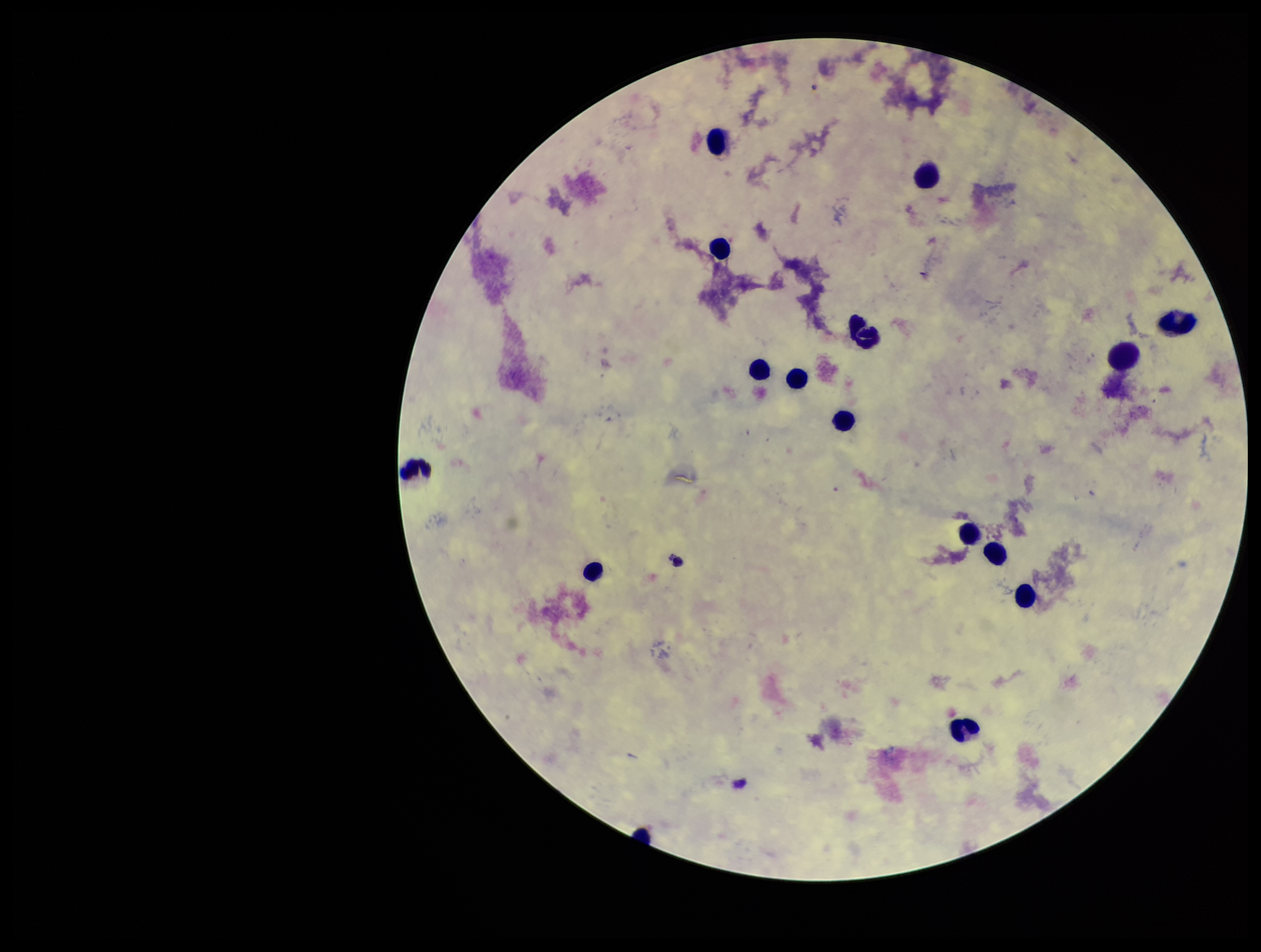
Summary:
  - Plasmodium parasites: none detected
  - Parasite count: 0
  - Capture: smartphone photograph through the microscope eyepiece
  - Stain: Giemsa
  - Field of view: one from this slide
  - Image size: 1261×952 pixels
  - Leukocyte count: 16
  - Patient malaria status: negative
  - Preparation: thick blood smear